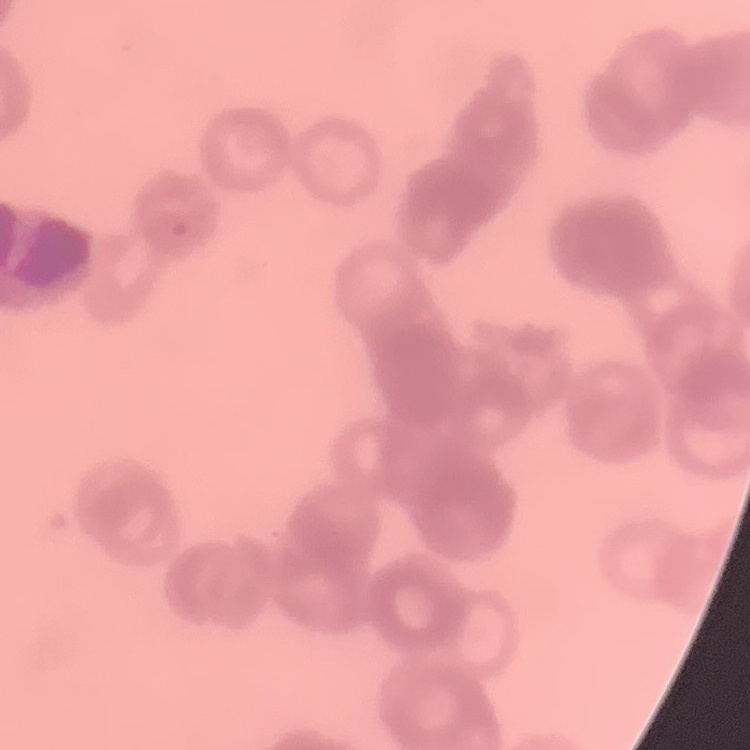

erythrocyte morphology = rouleaux formation
stain = Field's or Giemsa
preparation = thin peripheral smear
image type = square crop of a larger photomicrograph